State which cell type is depicted.
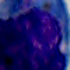
This is a leukocyte.

{
  "modality": "micrograph",
  "magnification": "1000x"
}